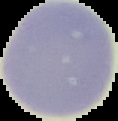

Image is 118×121 pixels. From a thin blood film. Malaria status: uninfected. Cell region segmented out of the field of view; the surrounding area is masked to black.